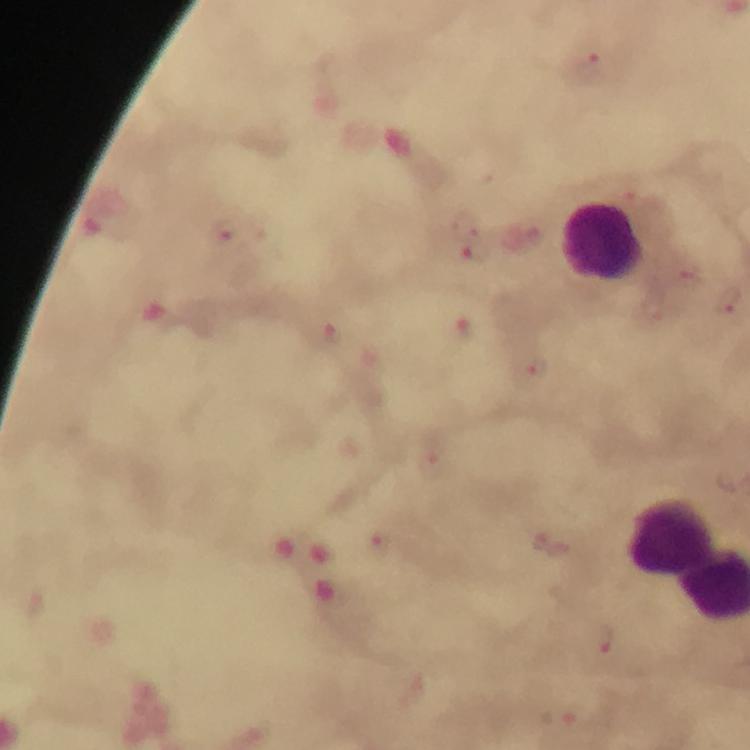
{
  "magnification": "100x",
  "stain": "Giemsa",
  "preparation": "thick blood film",
  "image_size": "750×750 pixels",
  "immersion_oil": "used",
  "leukocyte_locations": "approximate centers as (x, y) in pixels: (604, 243), (674, 539)",
  "cropped_from": "a single field of view",
  "capture": "smartphone photograph through a microscope",
  "context": "from a malaria diagnostic workup",
  "plasmodium_parasite_locations": "approximate centers as (x, y) in pixels: (592, 64), (227, 231), (689, 277), (730, 303), (461, 333), (328, 335), (532, 371), (379, 542), (603, 641)"
}